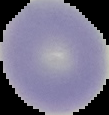
image type = segmented cell region on a black background
preparation = thin blood film
malaria status = uninfected
image size = 109×115 pixels